State which parasite is depicted.
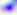
Toxoplasma gondii.

400x magnification. Micrograph.